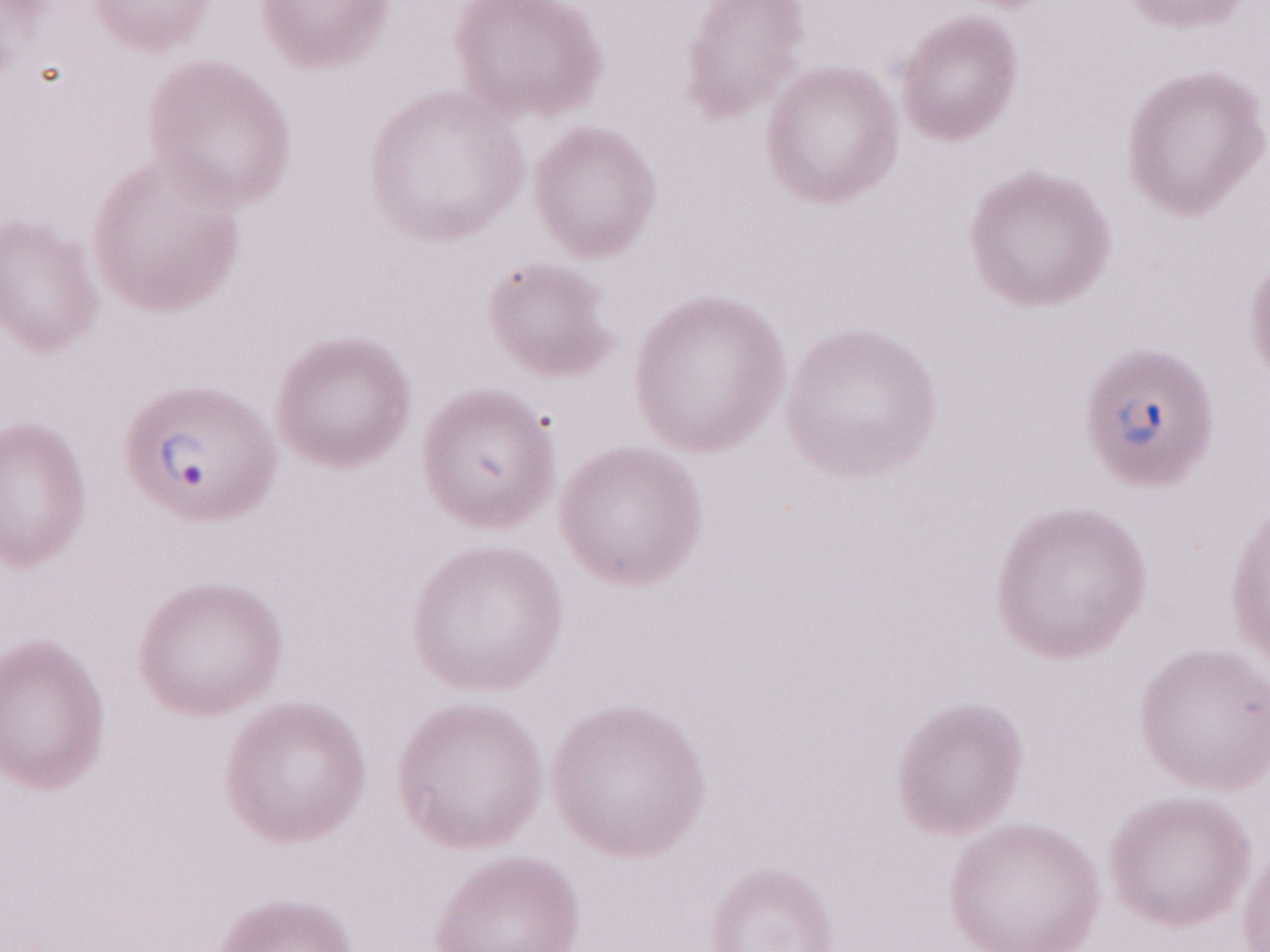

Patient diagnosis: malaria infection. One field of this slide. Magnification: 1,000x. Olympus BX43 microscope and DP73 digital camera. Thin blood film. Image is 1270×952 pixels. May-Grünwald-Giemsa (MGG) stain.